State which parasite is depicted.
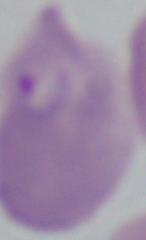

Babesia.

Captured at 1000x magnification. Micrograph.